Assess the morphology of the red blood cells.
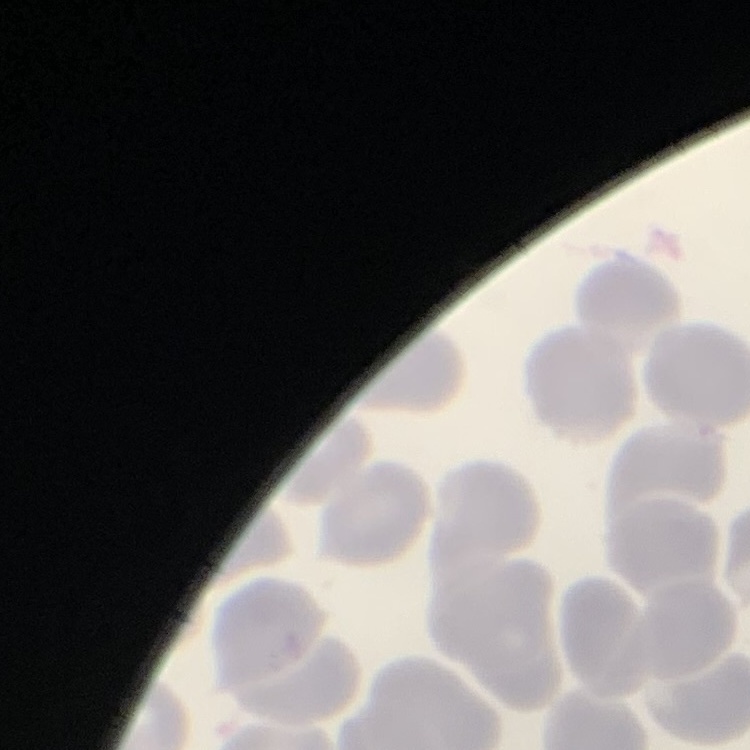
They show no rouleaux formation.

image type = square crop of a larger photomicrograph
stain = Field's or Giemsa
preparation = thin blood smear